Assess this cell for malaria.
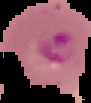
It is parasitized.

preparation: thin blood film
image_size: 91×103 pixels
image_type: segmented cell region on a black background